Outline each blood parasite and name the species.
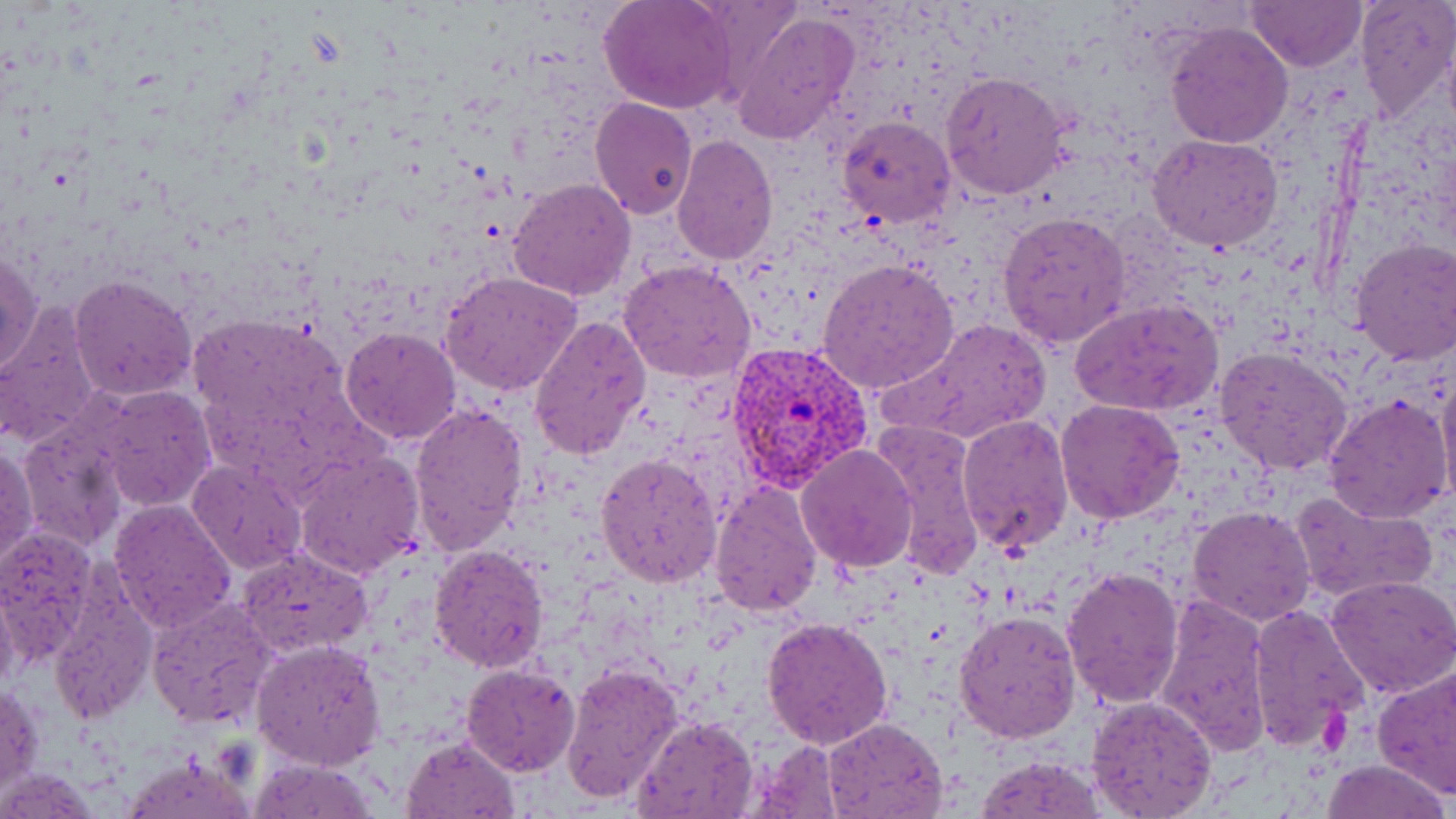
Approximate bounding boxes as (x1,y1)-(x2,y2) corner pairs in pixels.
Plasmodium vivax-infected red blood cells: (723,341)-(875,494).
No Plasmodium falciparum, Plasmodium ovale, Plasmodium malariae, Babesia divergens, or Trypanosoma brucei observed.

Summary:
  - Uninfected red blood cell locations: (1245,0)-(1366,72), (1352,0)-(1455,124), (600,2)-(734,113), (731,12)-(859,144), (1164,22)-(1295,150), (939,70)-(1071,200), (590,97)-(698,221), (836,116)-(955,230), (671,133)-(777,267), (1147,134)-(1283,254), (509,178)-(635,300), (999,209)-(1131,349), (1350,239)-(1456,364), (1,247)-(43,378), (818,257)-(958,397), (618,259)-(758,384), (441,270)-(581,395), (69,274)-(198,401), (1070,298)-(1223,416), (0,300)-(103,449), (528,314)-(652,460), (192,315)-(359,462), (891,316)-(1051,446), (339,327)-(460,444), (1213,345)-(1355,478), (1436,362)-(1456,505), (90,384)-(216,511), (1324,393)-(1455,525), (1055,398)-(1186,522), (409,402)-(527,556), (957,414)-(1074,557), (872,421)-(985,581), (19,422)-(130,551), (1,442)-(38,575), (796,444)-(920,573), (294,450)-(425,579), (594,452)-(724,589), (187,459)-(307,575), (710,479)-(824,615), (1290,489)-(1437,603), (108,499)-(237,633), (1187,503)-(1317,626), (0,524)-(100,664), (235,544)-(374,658), (429,544)-(551,672), (1061,565)-(1184,709), (1324,574)-(1456,698), (0,583)-(23,698), (45,585)-(155,723), (146,594)-(279,731), (1154,595)-(1274,755), (1245,603)-(1371,750), (953,608)-(1082,744), (761,616)-(894,749), (251,639)-(386,771), (461,662)-(580,776), (559,662)-(684,805), (1373,664)-(1456,800), (2,685)-(44,795), (1085,695)-(1218,818), (633,714)-(759,819), (820,717)-(950,819), (402,736)-(520,818), (747,739)-(846,817), (119,751)-(259,819), (975,756)-(1106,818), (249,758)-(381,818), (1321,758)-(1451,819)
  - Platelet locations: (1317,696)-(1352,754)
  - Slide-level diagnosis: Plasmodium vivax
  - Modality: light microscopy
  - Preparation: thin blood film
  - Magnification: 1000x
  - Field of view: one of a larger specimen
  - Image size: 1456×819 pixels
  - Stain: May-Grünwald-Giemsa